Point out each Plasmodium parasite.
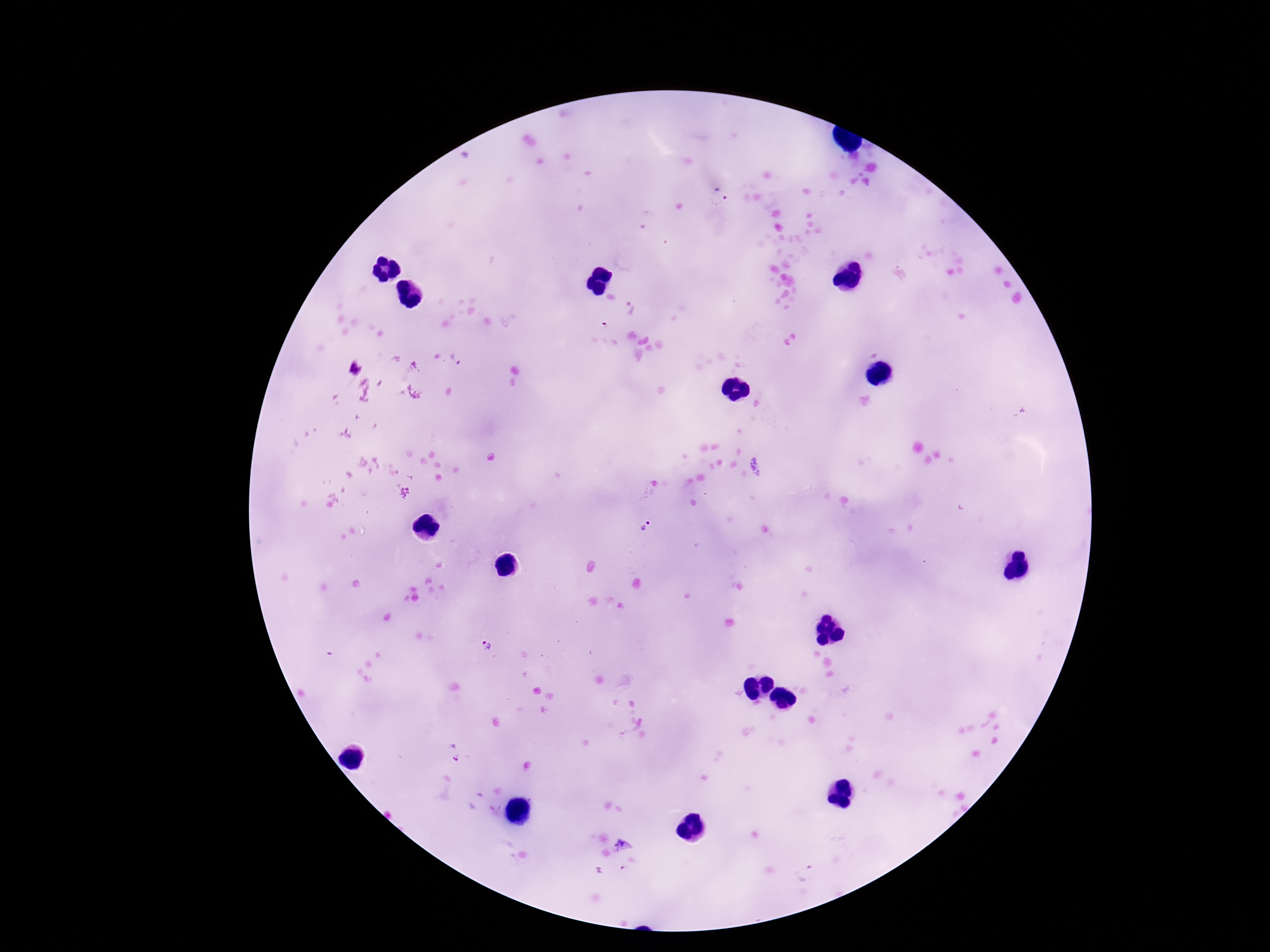

Approximate centers as {x, y} in pixels.
Plasmodium parasites: {721, 195}, {631, 308}, {456, 357}, {647, 525}, {485, 648}, {455, 752}, {622, 845}.

Summary:
  - Capture: smartphone camera through the microscope eyepiece
  - Stain: Giemsa
  - Preparation: thick blood smear
  - Patient malaria status: positive
  - Field of view: one from this slide
  - Image size: 1270×952 pixels
  - Magnification: 100x